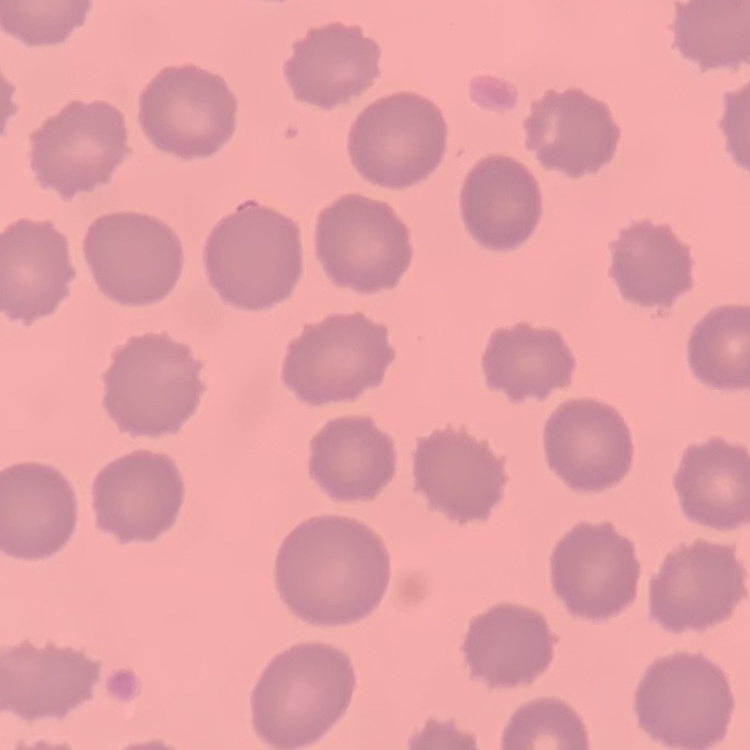
Summary:
  - Erythrocyte morphology: no rouleaux formation
  - Stain: Field's or Giemsa
  - Image type: one tile cut from a larger photomicrograph
  - Preparation: thin blood film